Name the parasite shown.
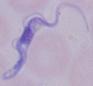

This is a trypanosome.

Summary:
  - Magnification: 1000x
  - Modality: micrograph